Classify this cell by malaria status.
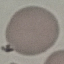
It is uninfected.

Summary:
  - Preparation: thin blood film
  - Capture: smartphone camera at the microscope eyepiece
  - Stain: Giemsa
  - Image type: cell patch, automatically extracted from a larger field of view and resized to 64 × 64 pixels